Name the blood parasite species.
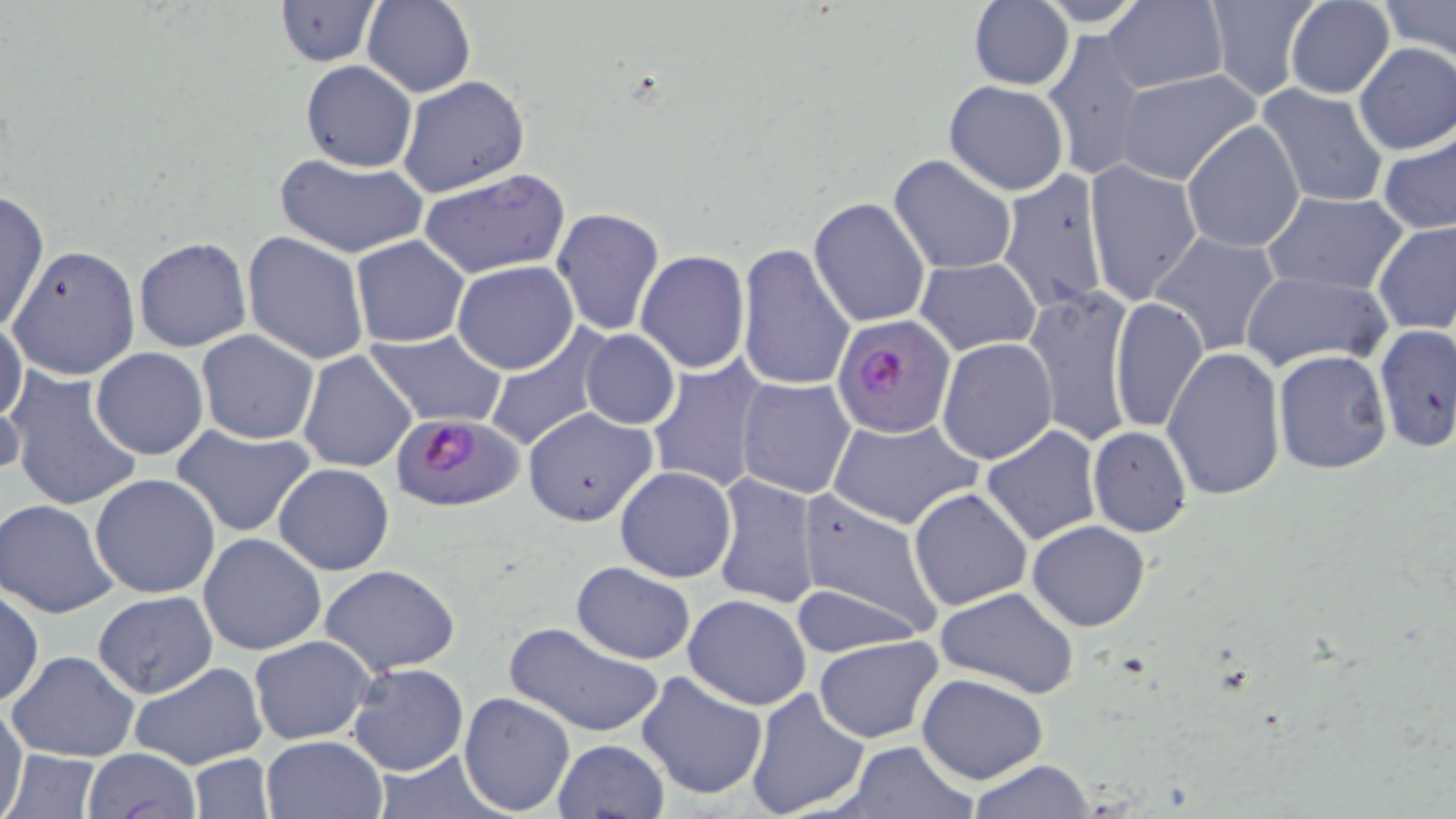

Plasmodium falciparum.

Summary:
  - Coordinate format: approximate bounding boxes as [x1, y1, x2, y2] in pixels
  - Plasmodium falciparum-infected red blood cell locations: [835, 319, 961, 443], [392, 413, 526, 513]
  - Uninfected red blood cell locations: [274, 0, 383, 66], [362, 0, 476, 97], [968, 0, 1074, 90], [1202, 0, 1320, 98], [1283, 0, 1397, 99], [1379, 0, 1456, 60], [1102, 1, 1227, 93], [1042, 28, 1149, 181], [1353, 43, 1456, 156], [301, 60, 416, 172], [1113, 69, 1262, 186], [398, 75, 530, 197], [943, 80, 1069, 196], [1258, 84, 1389, 208], [1182, 118, 1306, 253], [1378, 129, 1456, 236], [275, 153, 427, 258], [889, 153, 1018, 276], [1085, 160, 1202, 305], [997, 167, 1111, 314], [418, 168, 570, 279], [0, 190, 49, 334], [1262, 191, 1405, 295], [808, 196, 931, 327], [552, 207, 664, 335], [1373, 219, 1456, 335], [241, 230, 370, 364], [1151, 230, 1282, 358], [350, 236, 468, 348], [133, 237, 251, 352], [735, 242, 856, 394], [352, 245, 577, 358], [8, 246, 141, 380], [637, 249, 750, 374], [916, 257, 1041, 355], [452, 261, 578, 374], [1240, 270, 1391, 371], [1026, 287, 1137, 450], [1109, 295, 1208, 434], [0, 316, 28, 428], [1375, 323, 1455, 453], [482, 324, 610, 453], [365, 329, 508, 427], [581, 329, 679, 430], [196, 331, 320, 444], [935, 338, 1057, 465], [1162, 347, 1286, 500], [91, 348, 208, 460], [1273, 349, 1393, 475], [298, 351, 418, 474], [646, 357, 772, 494], [4, 366, 143, 513], [735, 377, 857, 500], [0, 386, 26, 486], [521, 407, 659, 528], [826, 416, 982, 532], [981, 423, 1103, 545], [172, 425, 316, 538], [1088, 426, 1192, 537], [274, 463, 395, 576], [615, 466, 738, 582], [711, 472, 822, 609], [89, 474, 220, 597], [908, 488, 1033, 611], [792, 490, 944, 639], [0, 498, 121, 618], [1026, 520, 1151, 633], [198, 533, 327, 657], [571, 562, 695, 664], [317, 565, 461, 676], [789, 582, 924, 659], [933, 586, 1081, 699], [0, 590, 44, 706], [92, 592, 217, 697], [684, 594, 810, 709], [503, 620, 667, 740], [250, 635, 376, 745], [815, 635, 946, 744], [8, 650, 140, 762], [130, 662, 268, 769], [346, 662, 469, 776], [636, 669, 768, 799], [917, 673, 1048, 785], [743, 688, 871, 819], [458, 691, 574, 813], [0, 700, 28, 819], [260, 735, 386, 819], [554, 739, 668, 818], [840, 740, 975, 818], [3, 748, 103, 819], [80, 748, 200, 817], [373, 749, 510, 817], [189, 752, 274, 817], [964, 759, 1098, 817]
  - Preparation: thin blood smear
  - Modality: light microscopy
  - Magnification: 1000x
  - Field of view: one of a larger specimen
  - Image size: 1456×819 pixels
  - Stain: May-Grünwald-Giemsa